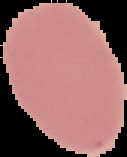

Summary:
  - Result: no Plasmodium parasites seen
  - Image size: 127×157 pixels
  - Preparation: thin blood film
  - Image type: segmented cell region with the area outside set to black